Assess this cell for malaria.
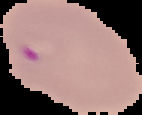
Parasitized.

From a thin blood smear. Cell region segmented out of the field of view; the surrounding area is masked to black. Image is 142×115 pixels.